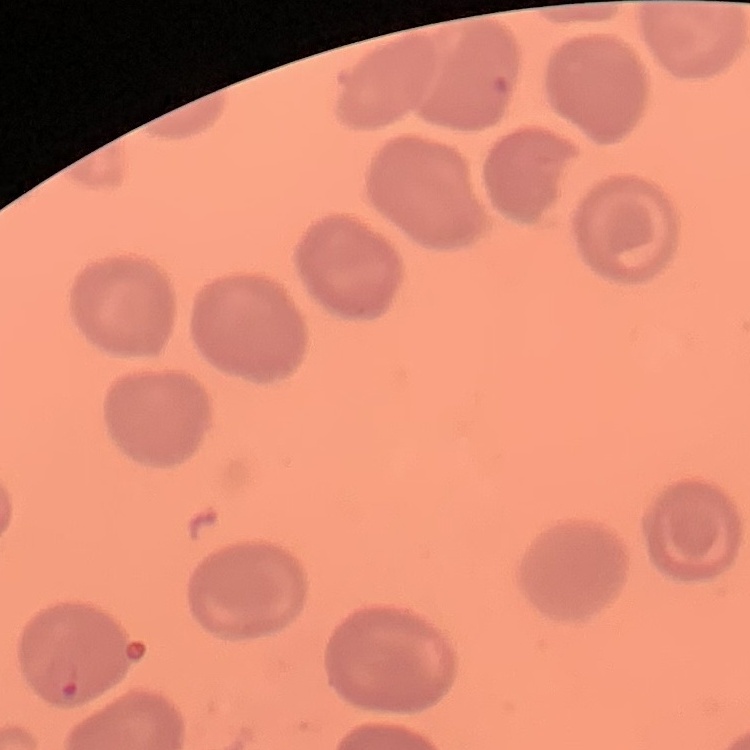 The red blood cells exhibit no rouleaux formation. One tile cut from a larger photomicrograph. Field's or Giemsa stain. Thin blood film.